Locate every blood parasite and identify its species.
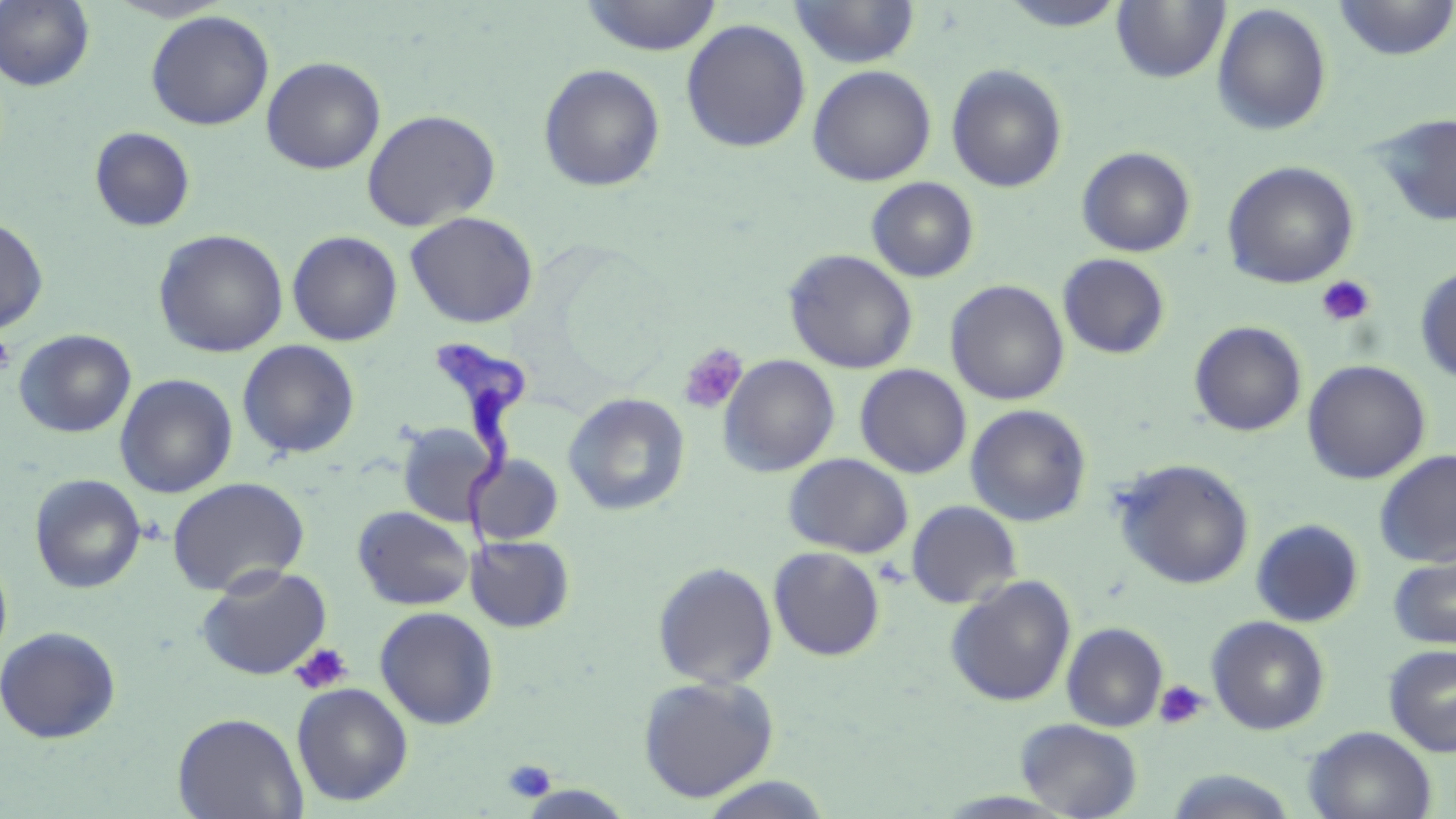

Approximate bounding boxes as (x1, y1, x2, y2) in pixels.
Trypanosoma brucei: (429, 338, 528, 576).
No Plasmodium falciparum, Plasmodium ovale, Plasmodium malariae, Plasmodium vivax, or Babesia divergens observed.

Platelet locations: (1316, 275, 1376, 327), (0, 332, 16, 377), (678, 343, 748, 414), (290, 643, 353, 695), (1154, 679, 1209, 730), (503, 759, 556, 804). Uninfected red blood cell locations: (0, 0, 95, 91), (105, 0, 233, 22), (579, 0, 723, 56), (789, 0, 920, 69), (996, 0, 1131, 32), (1112, 0, 1230, 84), (1332, 0, 1456, 61), (1212, 3, 1332, 136), (146, 10, 275, 131), (680, 18, 811, 154), (261, 57, 386, 175), (538, 63, 666, 192), (946, 64, 1068, 194), (807, 65, 936, 186), (362, 109, 501, 232), (1372, 112, 1456, 227), (89, 126, 196, 233), (1076, 146, 1196, 258), (1222, 160, 1359, 289), (866, 177, 979, 283), (404, 211, 539, 328), (0, 216, 49, 333), (153, 229, 289, 358), (286, 230, 403, 346), (784, 249, 918, 374), (1057, 253, 1170, 359), (1415, 265, 1456, 384), (946, 280, 1069, 406), (1189, 321, 1307, 437), (14, 329, 136, 438), (237, 340, 360, 460), (718, 354, 840, 477), (1302, 359, 1431, 484), (855, 364, 972, 479), (115, 373, 238, 498), (563, 393, 690, 517), (966, 404, 1092, 527), (397, 422, 497, 526), (1374, 449, 1456, 568), (467, 453, 564, 546), (784, 453, 913, 558), (1112, 459, 1254, 590), (29, 473, 146, 594), (167, 477, 310, 597), (906, 500, 1022, 609), (352, 506, 474, 611), (1251, 519, 1363, 627), (465, 534, 575, 633), (768, 547, 885, 661), (0, 552, 13, 669), (1388, 552, 1456, 650), (653, 561, 778, 689), (196, 564, 333, 681), (945, 575, 1076, 707), (374, 606, 499, 730), (1206, 616, 1330, 735), (1061, 622, 1168, 732), (0, 625, 121, 744), (1384, 644, 1456, 756), (637, 675, 779, 802), (292, 682, 413, 806), (172, 712, 307, 819), (1015, 718, 1143, 818), (1304, 726, 1436, 819), (1162, 769, 1300, 819), (696, 775, 834, 818). Slide-level diagnosis: Trypanosoma brucei. Captured at 1000x magnification. One field of a larger specimen. Image is 1456×819 pixels. May-Grünwald-Giemsa-stained preparation. Optical microscopy. Thin blood film.